State which cell type is depicted.
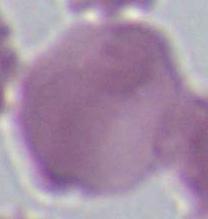

This is an erythrocyte.

Summary:
  - Modality: micrograph
  - Magnification: 1000x